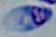

{
  "magnification": "1000x",
  "identification": "Toxoplasma gondii",
  "modality": "micrograph"
}